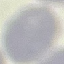

Malaria status: uninfected. Thin smear of blood. Giemsa stain. Acquired by smartphone through the microscope eyepiece. Cell patch, automatically extracted from a larger field of view and resized to 64 × 64 pixels.